Point out each malaria parasite.
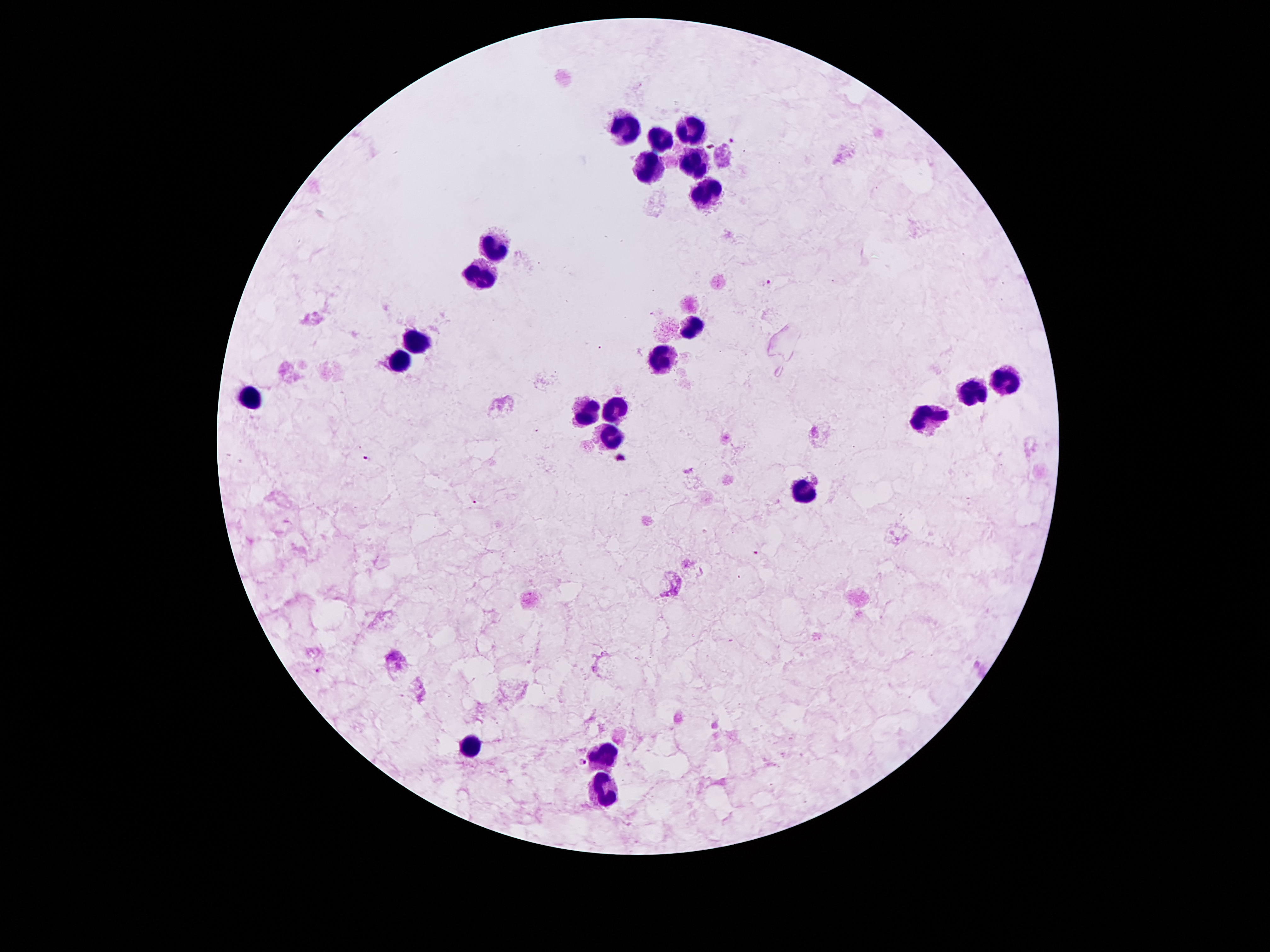
Approximate centers as [x, y] in pixels.
Malaria parasites: [734, 141], [768, 281], [623, 457], [369, 458], [476, 502], [756, 552], [320, 670], [581, 763].

Leukocyte locations: [697, 125], [624, 129], [659, 140], [698, 160], [650, 170], [708, 194], [495, 248], [478, 279], [691, 326], [416, 340], [400, 362], [663, 362], [1005, 379], [969, 392], [250, 401], [583, 414], [618, 414], [928, 416], [605, 435], [803, 491], [472, 753], [609, 753], [607, 789]. One field from this slide. Giemsa-stained preparation. Patient malaria status: positive for Plasmodium falciparum. 100x magnification. Smartphone photograph taken through the microscope eyepiece. Image is 1270×952 pixels. Thick peripheral-blood smear.